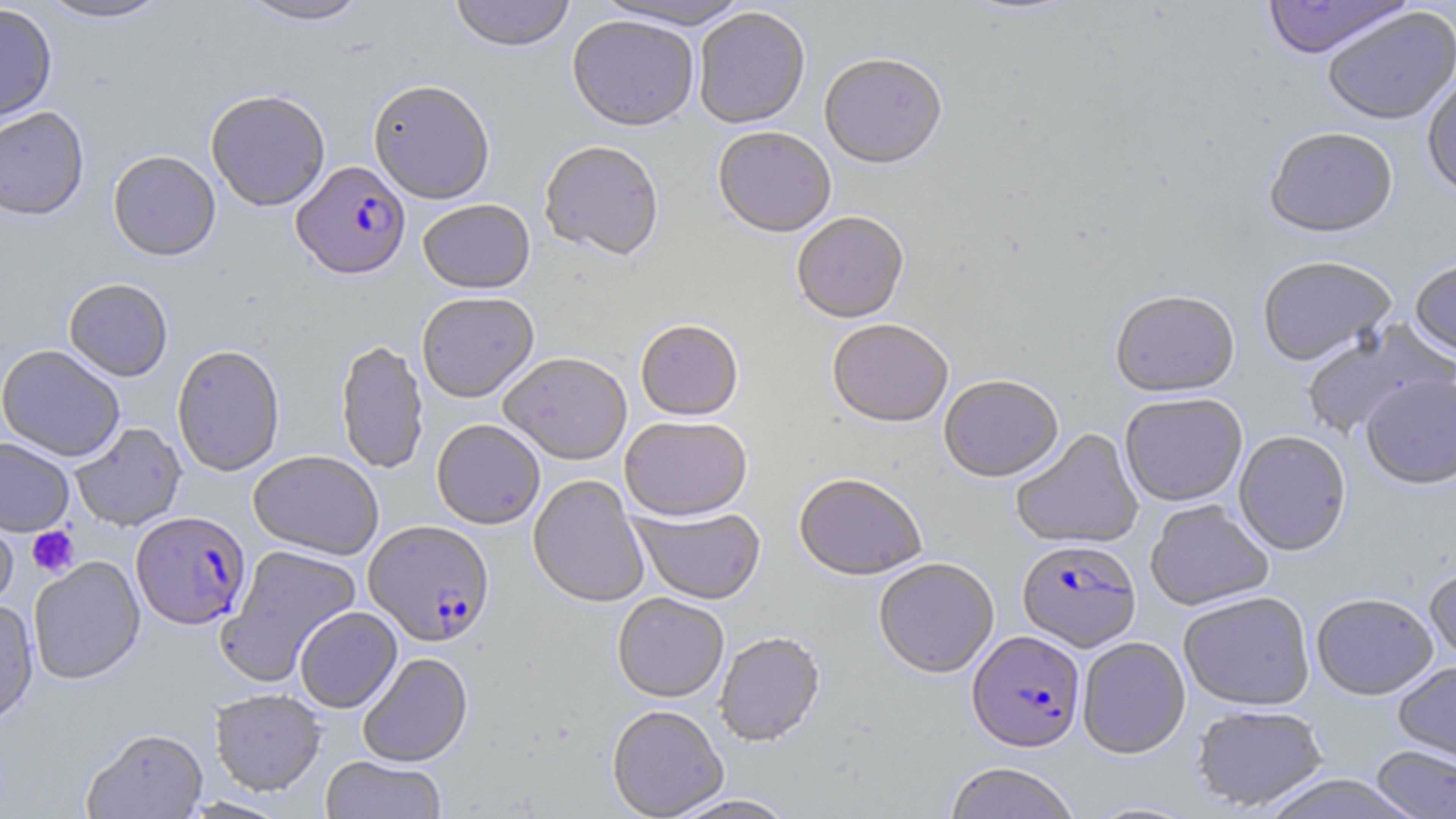
Summary:
  - Coordinate format: approximate bounding boxes as [x1, y1, x2, y2] in pixels
  - Uninfected red blood cell locations: [35, 0, 173, 24], [236, 0, 373, 27], [449, 0, 576, 54], [591, 0, 755, 33], [956, 0, 1085, 21], [1260, 0, 1414, 60], [0, 5, 57, 124], [1322, 8, 1456, 126], [694, 9, 811, 131], [567, 17, 699, 135], [819, 57, 947, 172], [1422, 72, 1456, 202], [368, 82, 495, 206], [206, 91, 330, 213], [0, 108, 90, 223], [713, 129, 836, 240], [1264, 130, 1399, 241], [539, 143, 664, 264], [108, 152, 221, 263], [418, 201, 536, 296], [791, 214, 909, 325], [1257, 258, 1397, 368], [1409, 260, 1456, 363], [63, 279, 173, 382], [1110, 292, 1240, 400], [417, 294, 539, 405], [827, 321, 953, 430], [1300, 321, 1450, 440], [635, 322, 744, 423], [335, 341, 429, 476], [0, 346, 125, 462], [172, 346, 285, 477], [499, 354, 632, 467], [1360, 373, 1456, 490], [939, 377, 1064, 485], [1120, 394, 1247, 508], [620, 417, 753, 523], [431, 421, 545, 530], [70, 422, 187, 532], [1011, 429, 1144, 550], [1234, 432, 1351, 557], [0, 437, 74, 536], [248, 451, 384, 561], [793, 474, 927, 582], [528, 475, 649, 610], [1145, 501, 1274, 612], [631, 507, 766, 606], [0, 511, 18, 611], [215, 544, 363, 686], [29, 558, 145, 685], [874, 559, 999, 679], [1424, 563, 1456, 670], [1178, 593, 1315, 711], [1311, 594, 1438, 702], [612, 595, 729, 704], [0, 600, 39, 727], [295, 607, 402, 713], [714, 633, 826, 747], [1077, 638, 1191, 760], [357, 652, 473, 768], [1393, 661, 1456, 770], [210, 689, 326, 797], [1191, 705, 1327, 813], [607, 706, 728, 819], [81, 728, 209, 819], [1371, 745, 1456, 819], [321, 756, 447, 819], [943, 763, 1081, 819], [1256, 774, 1423, 819], [663, 795, 800, 819], [177, 797, 293, 818]
  - Plasmodium falciparum-infected red blood cell locations: [291, 162, 411, 282], [131, 512, 251, 631], [363, 521, 495, 648], [1017, 540, 1141, 653], [968, 631, 1086, 754]
  - Platelet locations: [27, 526, 80, 577]
  - Slide-level diagnosis: Plasmodium falciparum
  - Stain: May-Grünwald-Giemsa
  - Field of view: one of a larger specimen
  - Image size: 1456×819 pixels
  - Modality: light microscopy
  - Magnification: 1000x
  - Preparation: thin blood smear